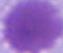 A red blood cell is shown. Captured at 1000x magnification. Photomicrograph.